Describe the morphology of the red blood cells.
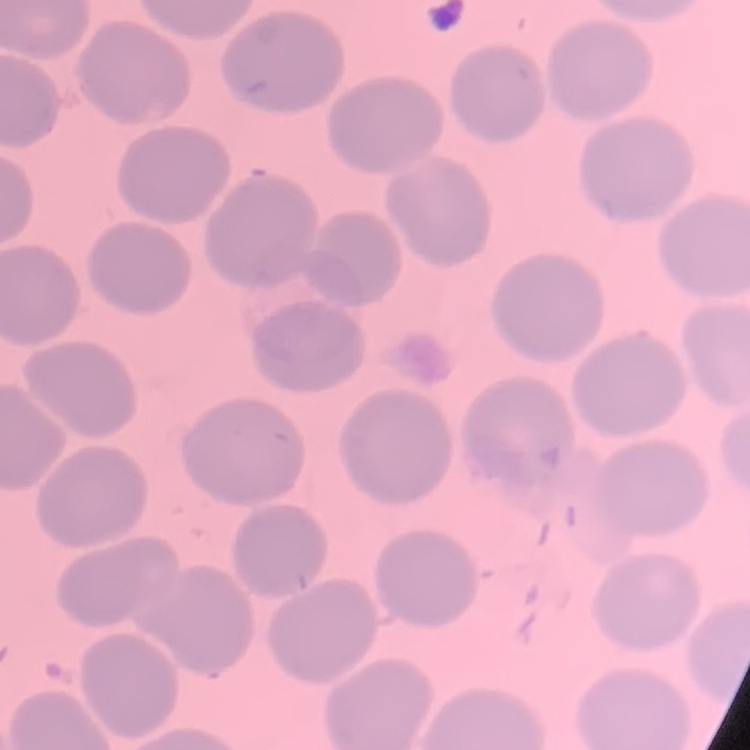
No rouleaux formation.

stain: Field's or Giemsa
preparation: thin peripheral smear
image_type: square crop of a larger photomicrograph